Report the malaria status of this cell.
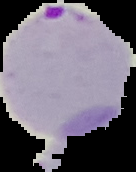

It is parasitized.

Image is 136×172 pixels. From a thin blood smear. Segmented cell region on a black background.